Give the extent of all Plasmodium ovale-infected red blood cells.
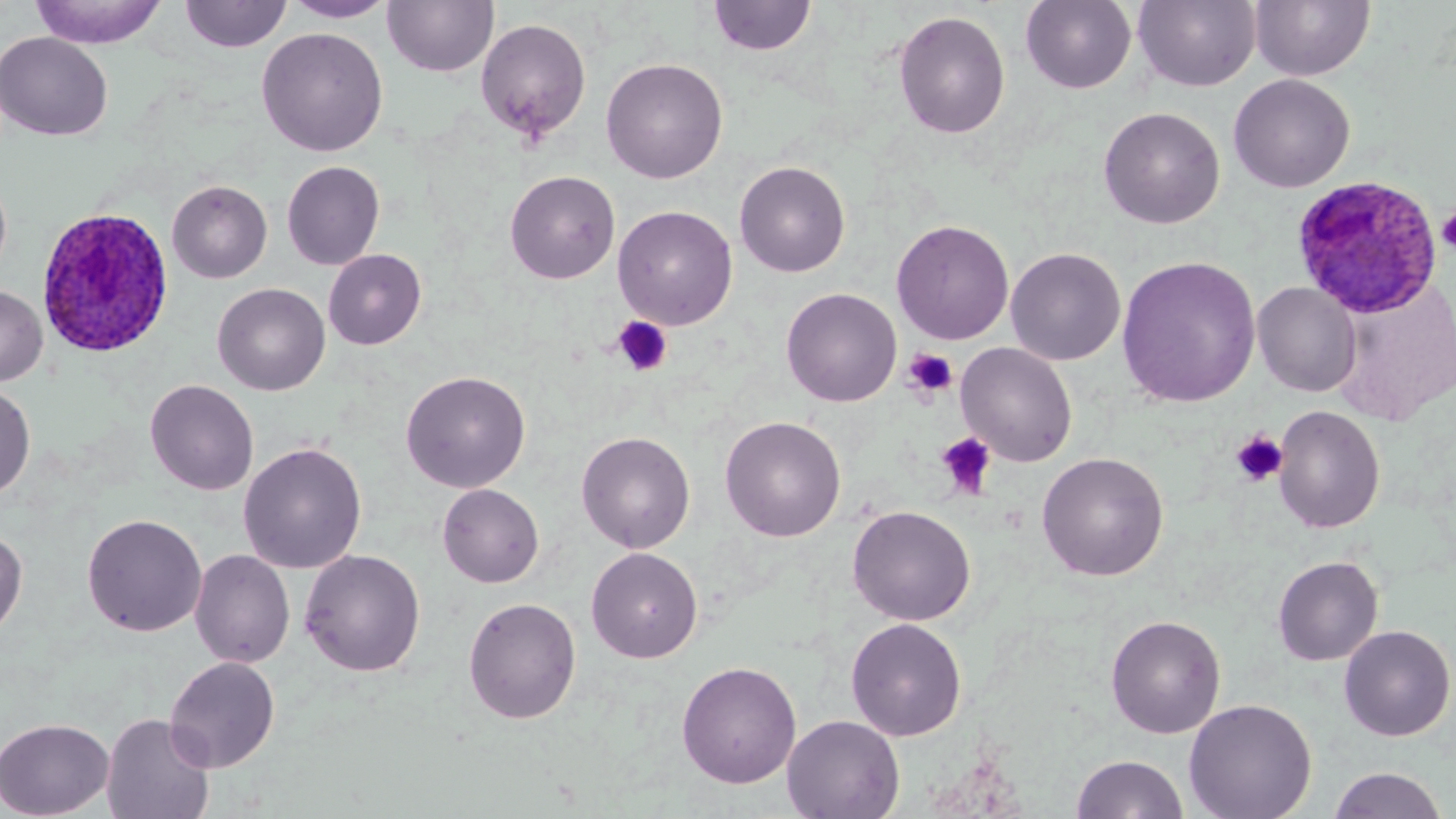
Approximate bounding boxes as named x1/y1/x2/y2 corners in pixels.
Plasmodium ovale-infected red blood cells: (x1=1291, y1=174, x2=1443, y2=319), (x1=36, y1=207, x2=174, y2=359).

Summary:
  - Platelet locations: (x1=1436, y1=207, x2=1456, y2=254), (x1=611, y1=316, x2=674, y2=377), (x1=903, y1=348, x2=958, y2=400), (x1=1231, y1=430, x2=1287, y2=486), (x1=936, y1=432, x2=998, y2=499)
  - Uninfected red blood cell locations: (x1=707, y1=0, x2=818, y2=58), (x1=1020, y1=0, x2=1137, y2=93), (x1=1133, y1=0, x2=1261, y2=92), (x1=1250, y1=0, x2=1375, y2=81), (x1=29, y1=1, x2=168, y2=48), (x1=179, y1=1, x2=293, y2=53), (x1=282, y1=1, x2=396, y2=23), (x1=383, y1=1, x2=499, y2=78), (x1=893, y1=10, x2=1011, y2=140), (x1=475, y1=17, x2=592, y2=142), (x1=256, y1=27, x2=388, y2=157), (x1=0, y1=31, x2=113, y2=141), (x1=600, y1=57, x2=729, y2=183), (x1=1228, y1=73, x2=1355, y2=193), (x1=1098, y1=106, x2=1225, y2=229), (x1=281, y1=160, x2=385, y2=270), (x1=734, y1=160, x2=851, y2=277), (x1=0, y1=169, x2=13, y2=285), (x1=504, y1=170, x2=620, y2=284), (x1=167, y1=180, x2=272, y2=283), (x1=612, y1=205, x2=738, y2=330), (x1=891, y1=219, x2=1014, y2=345), (x1=1005, y1=247, x2=1126, y2=366), (x1=323, y1=249, x2=426, y2=349), (x1=1116, y1=255, x2=1261, y2=407), (x1=1252, y1=281, x2=1362, y2=397), (x1=212, y1=283, x2=330, y2=396), (x1=0, y1=284, x2=48, y2=386), (x1=781, y1=287, x2=902, y2=407), (x1=955, y1=342, x2=1078, y2=467), (x1=400, y1=370, x2=531, y2=493), (x1=145, y1=378, x2=259, y2=496), (x1=0, y1=383, x2=36, y2=500), (x1=1272, y1=404, x2=1386, y2=533), (x1=719, y1=415, x2=846, y2=542), (x1=576, y1=431, x2=695, y2=553), (x1=238, y1=441, x2=367, y2=574), (x1=1037, y1=451, x2=1169, y2=581), (x1=437, y1=483, x2=544, y2=587), (x1=847, y1=505, x2=976, y2=626), (x1=82, y1=513, x2=207, y2=637), (x1=0, y1=526, x2=28, y2=642), (x1=586, y1=546, x2=703, y2=663), (x1=300, y1=548, x2=426, y2=677), (x1=189, y1=549, x2=295, y2=668), (x1=1272, y1=555, x2=1384, y2=666), (x1=463, y1=596, x2=582, y2=724), (x1=1105, y1=614, x2=1227, y2=738), (x1=846, y1=617, x2=967, y2=741), (x1=1338, y1=624, x2=1455, y2=741), (x1=164, y1=655, x2=280, y2=772), (x1=676, y1=660, x2=801, y2=788), (x1=1183, y1=698, x2=1317, y2=819), (x1=100, y1=712, x2=215, y2=819), (x1=781, y1=714, x2=905, y2=819), (x1=0, y1=717, x2=114, y2=818), (x1=1071, y1=753, x2=1189, y2=818), (x1=1327, y1=767, x2=1451, y2=818)
  - Slide-level diagnosis: Plasmodium ovale
  - Image size: 1456×819 pixels
  - Preparation: thin blood smear
  - Magnification: 1000x
  - Modality: light microscopy
  - Stain: May-Grünwald-Giemsa
  - Field of view: one of a larger specimen